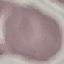
result = negative for malaria parasites
image type = cell patch, automatically extracted from a larger field of view and resized to 64 × 64 pixels
stain = Giemsa
capture = smartphone through the microscope eyepiece
preparation = thin blood film